Point out each Plasmodium parasite.
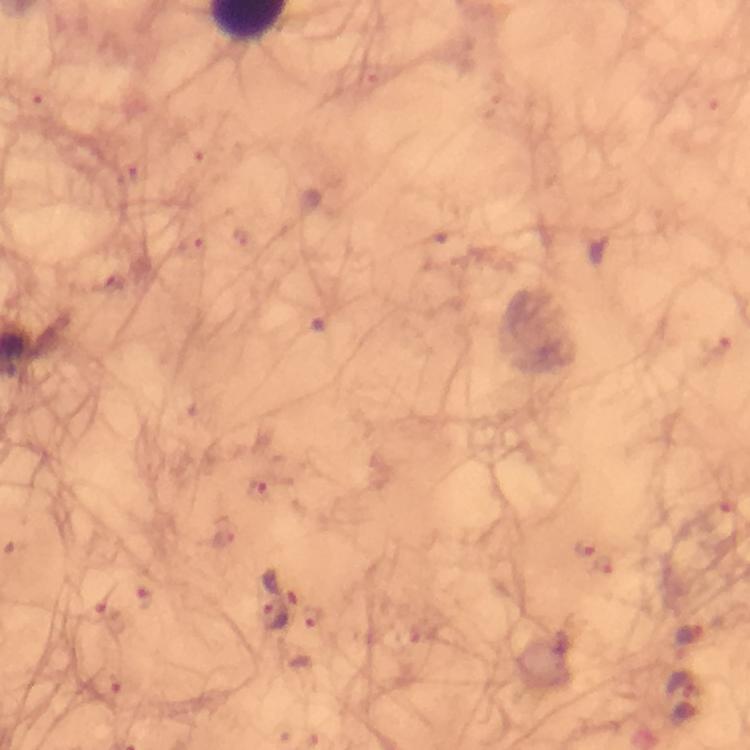

Approximate centers as [x, y] in pixels.
Plasmodium parasites: [716, 343], [257, 488], [720, 516], [583, 545], [281, 584], [143, 598], [107, 614], [274, 617].

cropped_from: a single field of view
context: from a malaria diagnostic workup
immersion_oil: used
preparation: thick smear
capture: smartphone camera through the microscope
magnification: 100x
stain: Giemsa
image_size: 750×750 pixels